Report the malaria status of this cell.
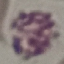

Uninfected.

Summary:
  - Stain: Giemsa
  - Preparation: thin blood smear
  - Capture: smartphone through the microscope eyepiece
  - Image type: automatically extracted cell patch, resized to 64 × 64 pixels